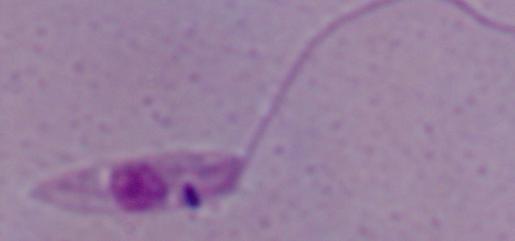

modality: micrograph
identification: Leishmania
magnification: 1000x